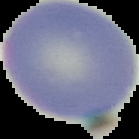 Image is 139×139 pixels. From a thin blood film. Malaria status: uninfected. The area outside the segmented cell region is set to black.